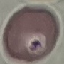
Malaria status: uninfected. Cell patch, automatically extracted from a larger field of view and resized to 64 × 64 pixels. Giemsa stain. Acquired by smartphone through the microscope eyepiece. Thin blood smear.